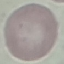
Summary:
  - Result: negative for malaria parasites
  - Image type: cell patch, automatically extracted from a larger field of view and resized to 64 × 64 pixels
  - Stain: Giemsa
  - Capture: smartphone camera at the microscope eyepiece
  - Preparation: thin blood film